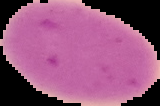
result: negative for Plasmodium parasites
preparation: thin blood smear
image_size: 160×106 pixels
image_type: cell region segmented out of the field of view; surrounding area masked to black